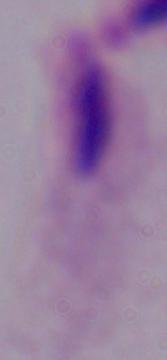

1000x magnification. A trichomonad is seen. Micrograph.